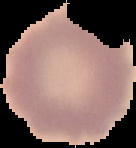
{
  "malaria_status": "uninfected",
  "image_type": "cell region segmented out of the field of view; surrounding area masked to black",
  "image_size": "136×148 pixels",
  "preparation": "thin blood smear"
}